Give the position of every malaria parasite.
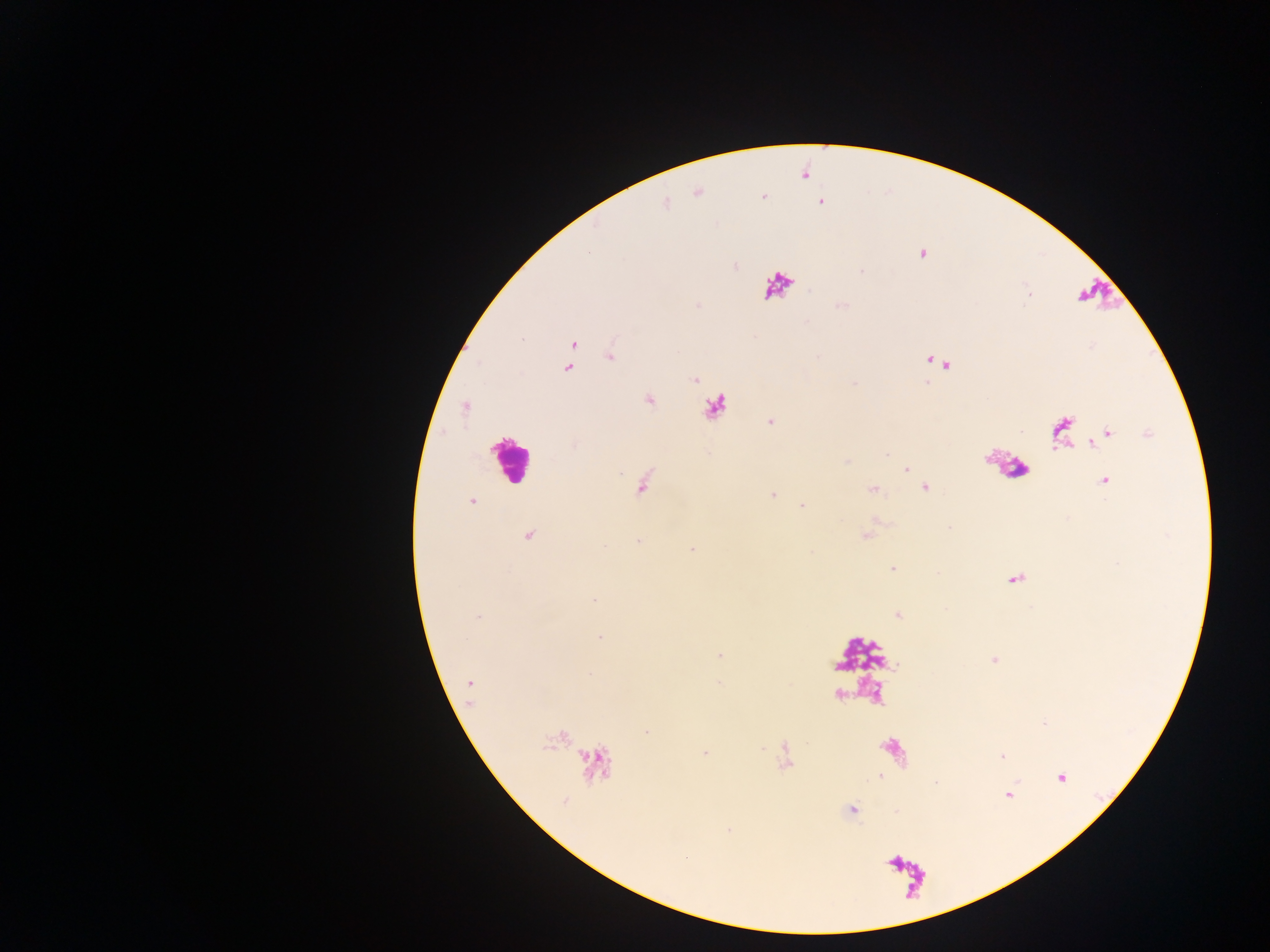

Approximate centers as {x, y} in pixels.
Malaria parasites: {820, 201}, {921, 253}, {572, 344}, {610, 355}, {569, 367}, {694, 380}, {649, 400}, {466, 407}, {771, 421}, {1103, 437}, {886, 455}, {906, 469}, {1105, 480}, {925, 487}, {873, 490}, {773, 494}, {472, 501}, {803, 505}, {529, 536}, {637, 541}, {692, 548}, {892, 569}, {594, 600}, {898, 615}, {478, 617}, {599, 637}, {719, 655}, {995, 660}, {589, 673}, {469, 682}, {718, 683}, {645, 730}, {705, 753}, {1001, 755}, {785, 763}, {881, 776}, {1062, 778}, {935, 782}, {1008, 795}, {852, 810}.

Leukocyte locations: {715, 407}, {509, 458}. Thick blood film. Photographed through a microscope with a mobile-phone camera. Collected in Ghana. Image is 1270×952 pixels. Single field of view.